Locate every Plasmodium ovale-infected red blood cell.
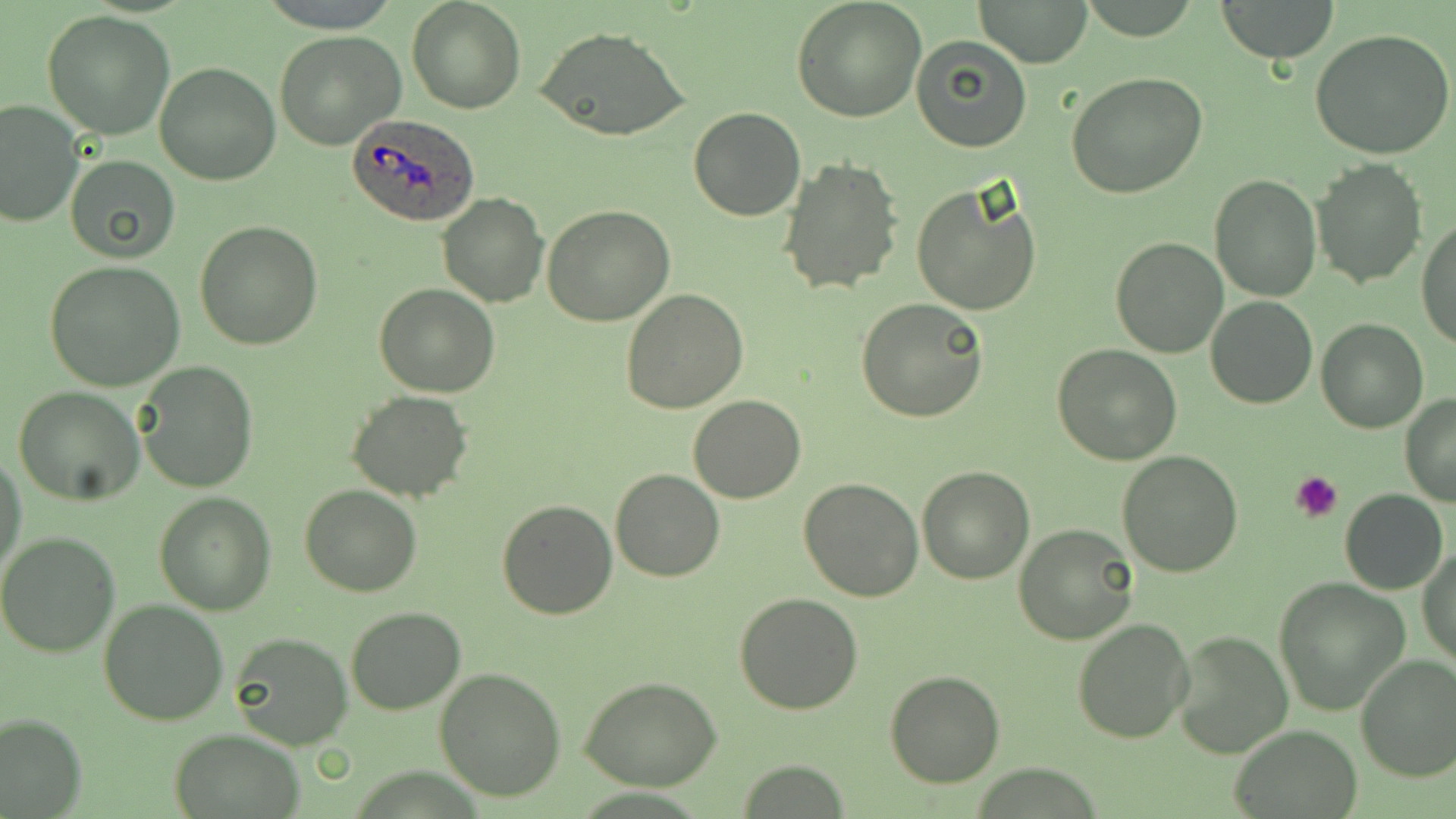
Approximate bounding boxes as [x1, y1, x2, y2] in pixels.
Plasmodium ovale-infected red blood cells: [344, 114, 481, 226].

Uninfected red blood cell locations: [408, 0, 524, 114], [793, 0, 926, 122], [974, 0, 1092, 68], [1215, 0, 1341, 62], [42, 9, 177, 139], [534, 26, 691, 144], [1310, 28, 1456, 161], [273, 30, 405, 150], [911, 36, 1031, 152], [153, 61, 281, 185], [1065, 71, 1208, 198], [1, 100, 82, 228], [688, 107, 808, 221], [64, 155, 180, 262], [774, 157, 904, 296], [1313, 159, 1426, 288], [1209, 175, 1320, 300], [911, 182, 1043, 317], [437, 192, 549, 307], [541, 205, 675, 327], [1416, 216, 1456, 350], [195, 221, 324, 351], [1111, 235, 1228, 357], [46, 260, 185, 390], [374, 283, 500, 398], [621, 288, 749, 413], [1205, 295, 1318, 409], [857, 298, 989, 423], [1316, 319, 1428, 435], [1052, 343, 1182, 466], [137, 364, 258, 491], [13, 384, 146, 506], [346, 390, 474, 501], [1399, 394, 1456, 506], [687, 395, 806, 503], [1, 451, 28, 582], [1116, 451, 1244, 576], [917, 466, 1035, 584], [611, 469, 724, 581], [799, 479, 924, 602], [299, 485, 423, 597], [1341, 490, 1448, 595], [153, 491, 277, 614], [497, 500, 619, 620], [1014, 523, 1140, 644], [0, 532, 121, 658], [1418, 543, 1455, 669], [1273, 577, 1409, 713], [733, 594, 863, 715], [98, 600, 228, 726], [344, 606, 467, 714], [1070, 616, 1195, 743], [1171, 630, 1293, 759], [228, 633, 350, 750], [1355, 654, 1456, 782], [433, 667, 567, 801], [883, 672, 1004, 788], [579, 677, 722, 790], [0, 713, 85, 818], [1232, 726, 1360, 818], [170, 728, 303, 817]. Platelet locations: [1291, 469, 1346, 520]. Slide-level diagnosis: Plasmodium ovale. 1000x magnification. Thin blood smear. Light microscopy. May-Grünwald-Giemsa-stained preparation. Image is 1456×819 pixels. Single field of view.